Report the malaria status of this cell.
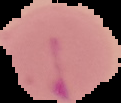
It is parasitized.

Summary:
  - Image type: cell region segmented out of the field of view; surrounding area masked to black
  - Preparation: thin blood smear
  - Image size: 121×103 pixels